Assess this cell for malaria.
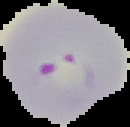
It is parasitized.

preparation = thin blood smear
image type = segmented cell region with the area outside set to black
image size = 130×127 pixels